Classify this cell by malaria status.
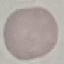
Uninfected.

Photographed with a smartphone camera at the microscope eyepiece. Cell patch, automatically extracted from a larger field of view and resized to 64 × 64 pixels. Giemsa stain. Thin blood smear.